Report the malaria status of this cell.
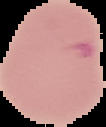
It is parasitized.

Segmented cell region on a black background. From a thin blood film. Image is 106×127 pixels.